Report the malaria status of this cell.
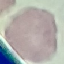

Uninfected.

stain: Giemsa
capture: smartphone through the microscope eyepiece
preparation: thin blood smear
image_type: cell patch, automatically extracted from a larger field of view and resized to 64 × 64 pixels